Report the malaria status of this cell.
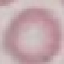

Uninfected.

Thin smear of blood. Acquired by smartphone through the microscope eyepiece. Automatically extracted cell patch, resized to 64 × 64 pixels. Giemsa stain.